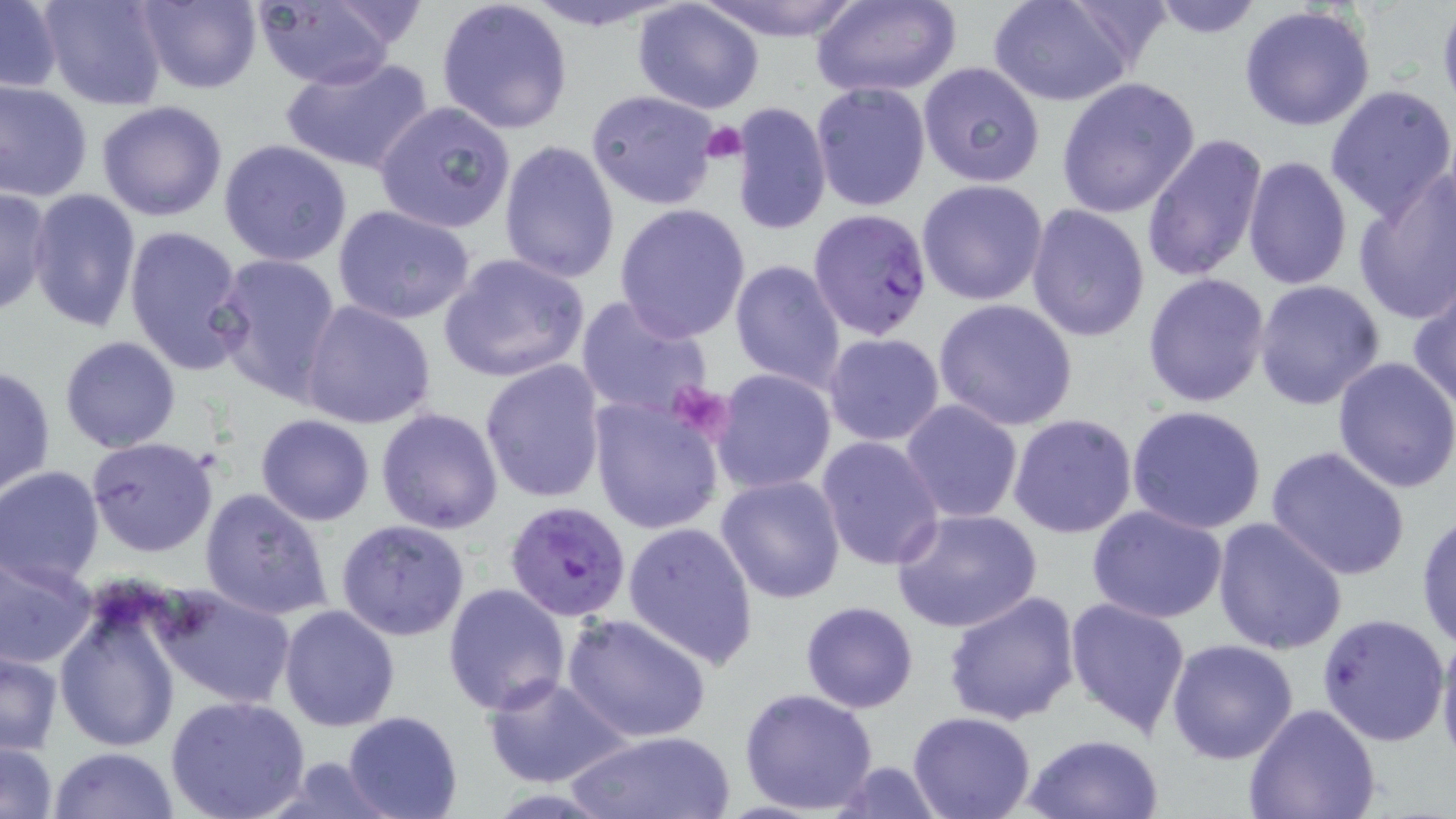
Summary:
  - Coordinate format: approximate bounding boxes as (x1,y1)-(x2,y2) corner pairs in pixels
  - Uninfected red blood cell locations: (38,0)-(169,111), (132,0)-(263,93), (244,0)-(403,90), (435,0)-(573,136), (515,0)-(690,30), (695,0)-(866,41), (809,0)-(962,99), (990,0)-(1140,108), (1145,0)-(1269,39), (0,2)-(62,93), (631,2)-(767,115), (1239,5)-(1377,132), (279,53)-(435,175), (916,62)-(1046,189), (1057,77)-(1201,219), (0,79)-(94,202), (809,81)-(930,214), (1324,85)-(1456,222), (585,89)-(724,211), (97,99)-(229,222), (374,100)-(518,235), (730,102)-(832,235), (1140,130)-(1270,285), (497,139)-(621,285), (218,140)-(353,267), (1242,155)-(1353,291), (1352,170)-(1456,326), (916,179)-(1050,306), (0,185)-(52,318), (26,189)-(141,333), (1024,203)-(1150,343), (331,204)-(479,326), (613,204)-(750,342), (122,224)-(248,376), (212,253)-(344,405), (438,253)-(591,383), (729,259)-(846,393), (1142,273)-(1273,409), (1408,278)-(1456,412), (1252,279)-(1385,411), (575,295)-(715,424), (933,299)-(1080,430), (299,300)-(438,429), (823,333)-(945,445), (59,336)-(182,454), (1333,355)-(1456,494), (479,358)-(607,503), (0,364)-(56,498), (711,369)-(838,495), (587,393)-(725,536), (900,399)-(1024,524), (1127,405)-(1268,536), (376,407)-(504,534), (255,413)-(376,526), (1007,413)-(1138,538), (229,434)-(362,578), (86,436)-(219,556), (816,436)-(944,573), (1263,443)-(1411,582), (0,467)-(105,587), (716,474)-(847,603), (198,486)-(335,621), (1085,505)-(1229,623), (890,506)-(1043,634), (1415,508)-(1456,652), (1212,516)-(1349,655), (335,518)-(472,643), (622,521)-(758,668), (0,552)-(97,670), (441,583)-(571,717), (152,584)-(296,710), (940,588)-(1081,725), (54,594)-(182,753), (1064,596)-(1192,738), (799,600)-(920,714), (278,604)-(402,733), (563,612)-(712,743), (1316,612)-(1450,746), (1434,627)-(1456,766), (1166,638)-(1298,763), (0,652)-(64,754), (482,673)-(631,789), (738,687)-(879,813), (165,694)-(313,819), (1245,703)-(1382,819), (343,711)-(463,819), (906,711)-(1036,819), (566,730)-(734,818), (1022,732)-(1165,819), (1,738)-(60,818), (50,747)-(181,819), (262,756)-(407,818), (827,760)-(947,818)
  - Plasmodium falciparum-infected red blood cell locations: (807,207)-(933,342), (506,501)-(632,621)
  - Platelet locations: (699,120)-(748,165), (663,384)-(734,444)
  - Slide-level diagnosis: Plasmodium falciparum
  - Preparation: thin blood film
  - Stain: May-Grünwald-Giemsa
  - Image size: 1456×819 pixels
  - Modality: light microscopy
  - Field of view: single
  - Magnification: 1000x